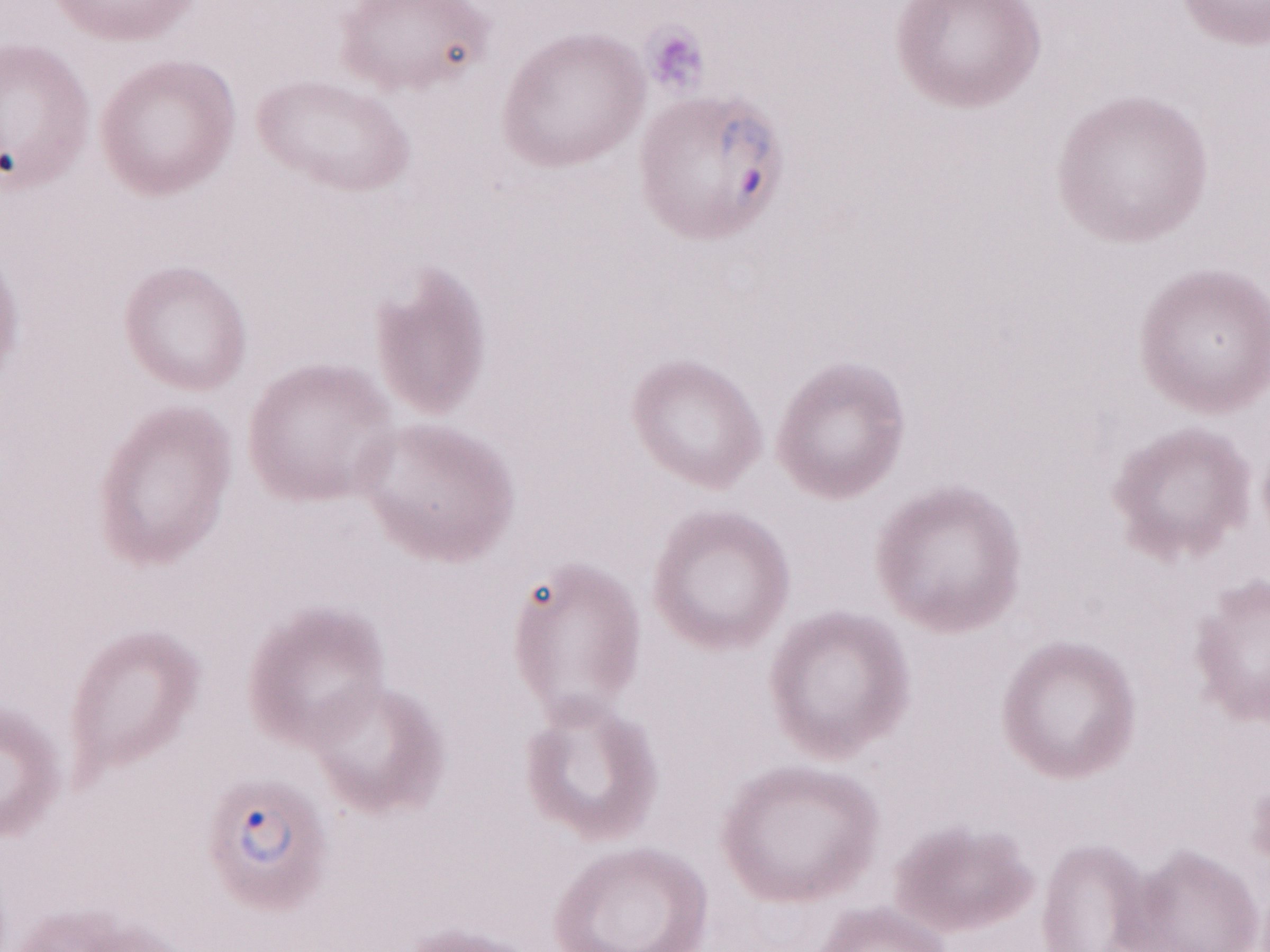 May-Grünwald-Giemsa (MGG) stain. Image is 1270×952 pixels. Olympus BX43 microscope and DP73 digital camera. One field of this slide. Thin blood smear. 1,000x magnification. Patient diagnosis: malaria infection.